Classify this cell by malaria status.
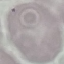
It is uninfected.

Summary:
  - Capture: smartphone camera at the microscope eyepiece
  - Image type: cell patch, automatically extracted from a larger field of view and resized to 64 × 64 pixels
  - Preparation: thin blood film
  - Stain: Giemsa